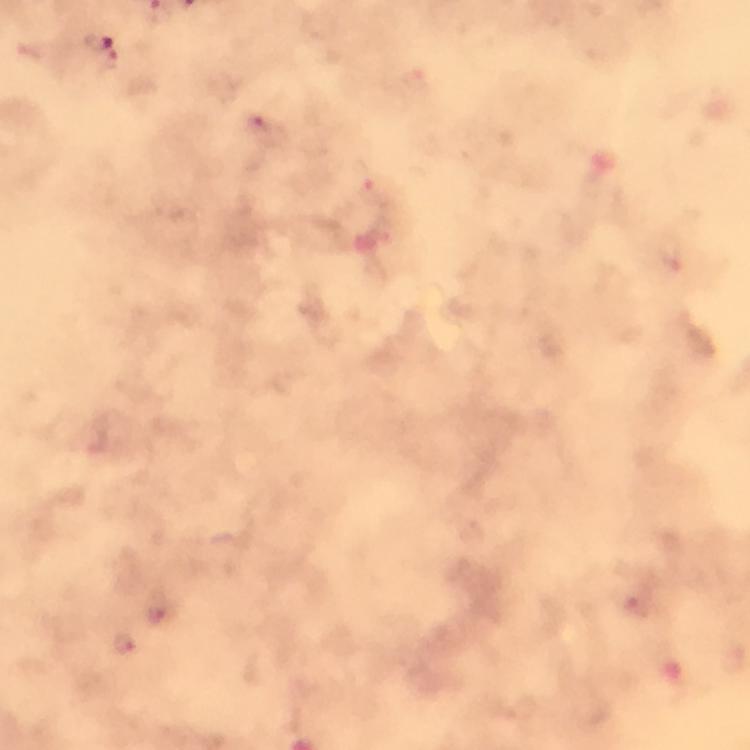 Approximate object centers, in pixels from the top-left corner. Malaria parasite locations: (x=98, y=42), (x=262, y=128), (x=158, y=607), (x=126, y=644). Giemsa-stained preparation. Thick blood smear. From a malaria diagnostic workup. Smartphone photograph taken through a microscope. A crop from one field of view. Image is 750×750 pixels. 100x magnification. Immersion oil was used.